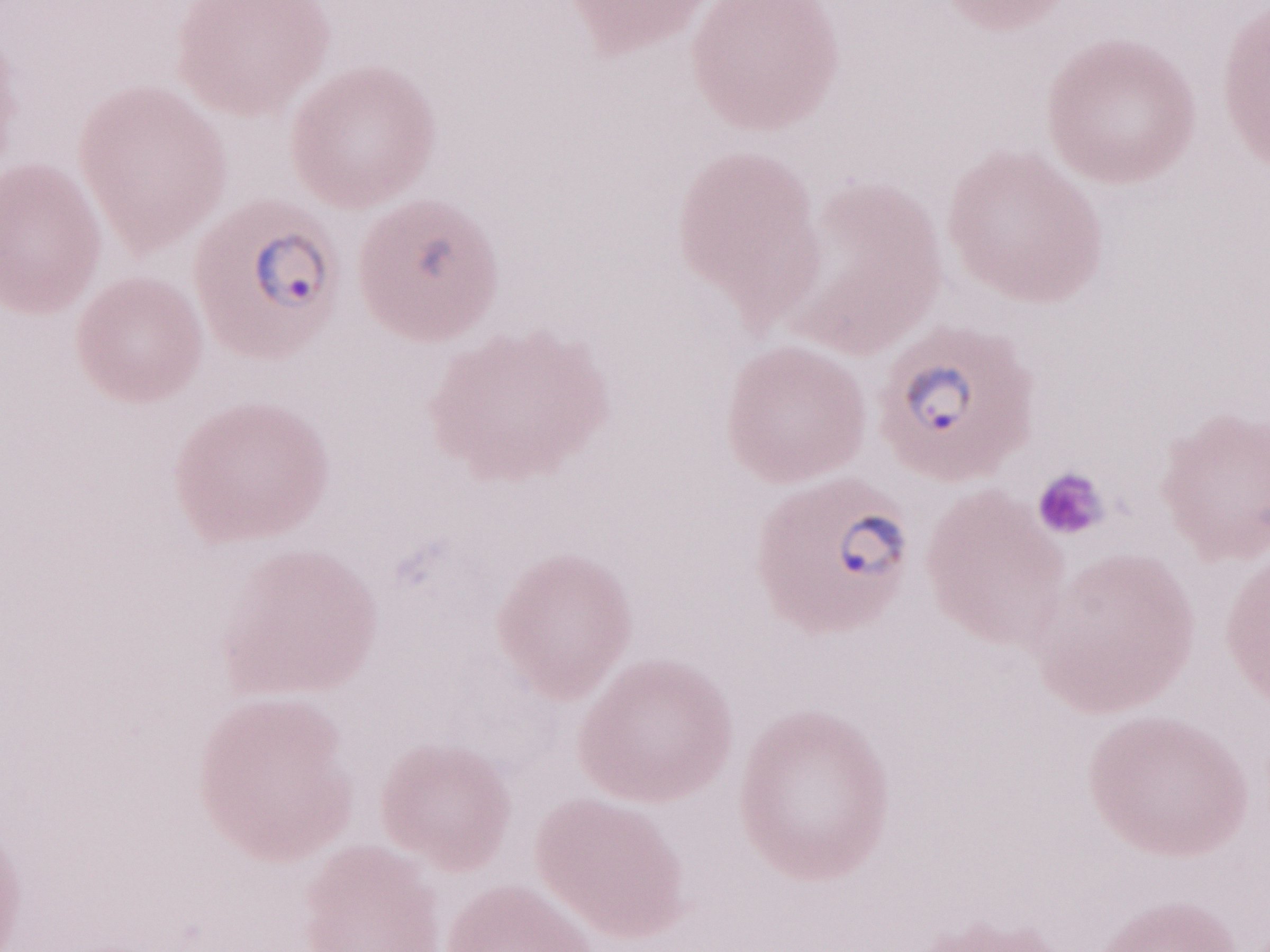 Single field of view. Image is 1270×952 pixels. 1,000x magnification. Patient-level malaria diagnosis: positive. May-Grünwald-Giemsa (MGG) stain. Olympus BX43 microscope, Olympus DP73 camera. Thin blood smear.